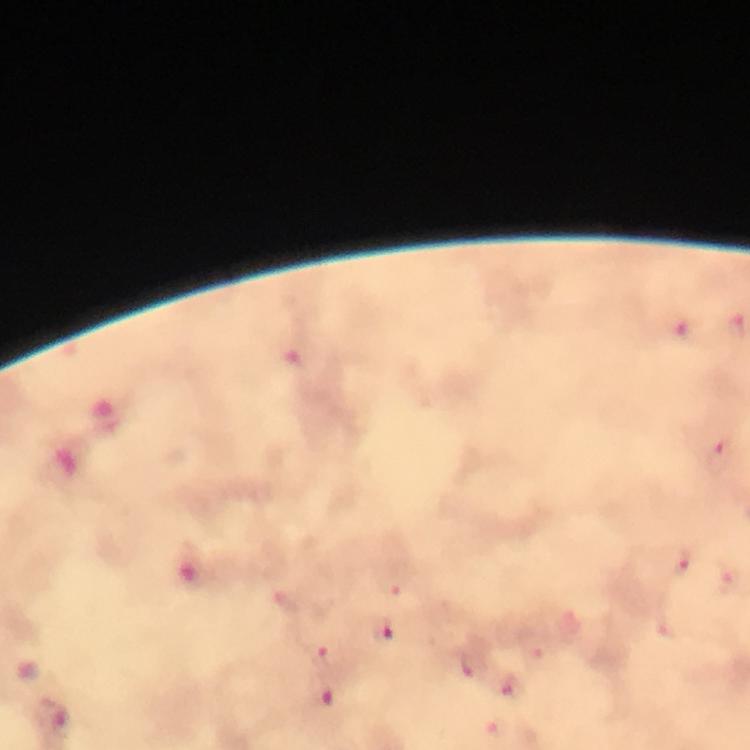

Approximate centers as (x, y) in pixels. Malaria parasite locations: (736, 326), (690, 330), (719, 454), (680, 564), (730, 581), (383, 628), (328, 655), (472, 667), (513, 686), (59, 723). Image is 750×750 pixels. Photographed with a smartphone mounted on the microscope. Thick blood film. A crop from one field of view. From a diagnostic examination for malaria. At 100x magnification. Giemsa stain. Immersion oil was used.